Classify this cell by malaria status.
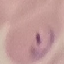
Parasitized.

Summary:
  - Stain: Giemsa
  - Preparation: thin blood smear
  - Capture: smartphone through the microscope eyepiece
  - Image type: cell patch, automatically extracted from a larger field of view and resized to 64 × 64 pixels